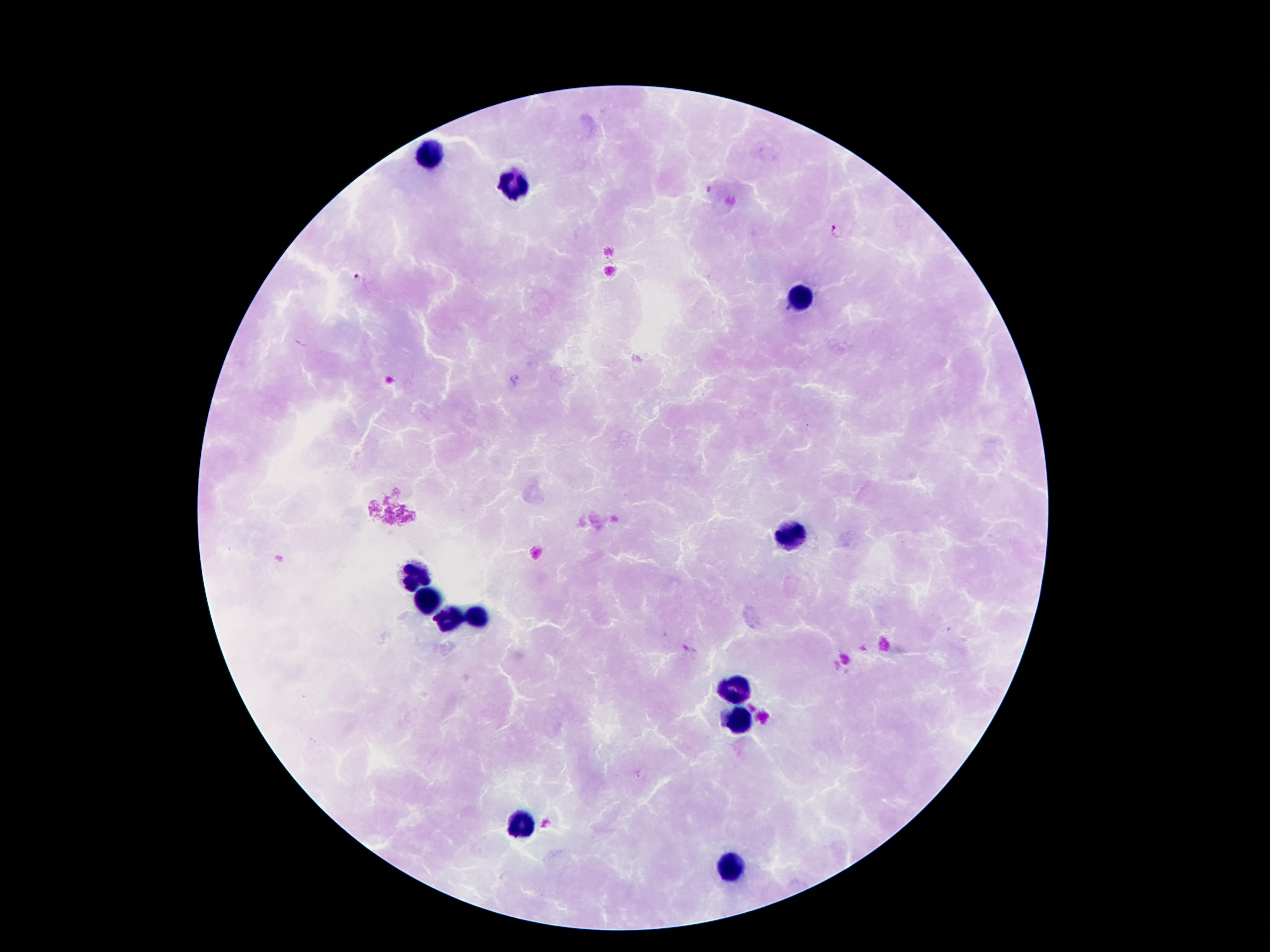
coordinate format = approximate centers as [x, y] in pixels
leukocyte locations = [430, 158], [512, 187], [804, 300], [795, 536], [414, 578], [430, 603], [476, 614], [450, 623], [731, 693], [737, 718], [525, 819], [735, 866]
malaria parasite locations = [836, 231], [359, 280]
capture = smartphone camera through the microscope eyepiece
field of view = single
image size = 1270×952 pixels
patient malaria status = positive for Plasmodium falciparum
stain = Giemsa
preparation = thick peripheral-blood smear
magnification = 100x